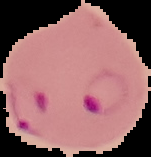
Image is 151×157 pixels. Malaria status: parasitized. From a thin blood smear. The area outside the segmented cell region is set to black.